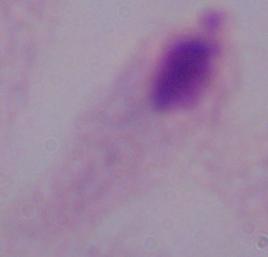

{
  "identification": "trichomonad",
  "magnification": "1000x",
  "modality": "photomicrograph"
}